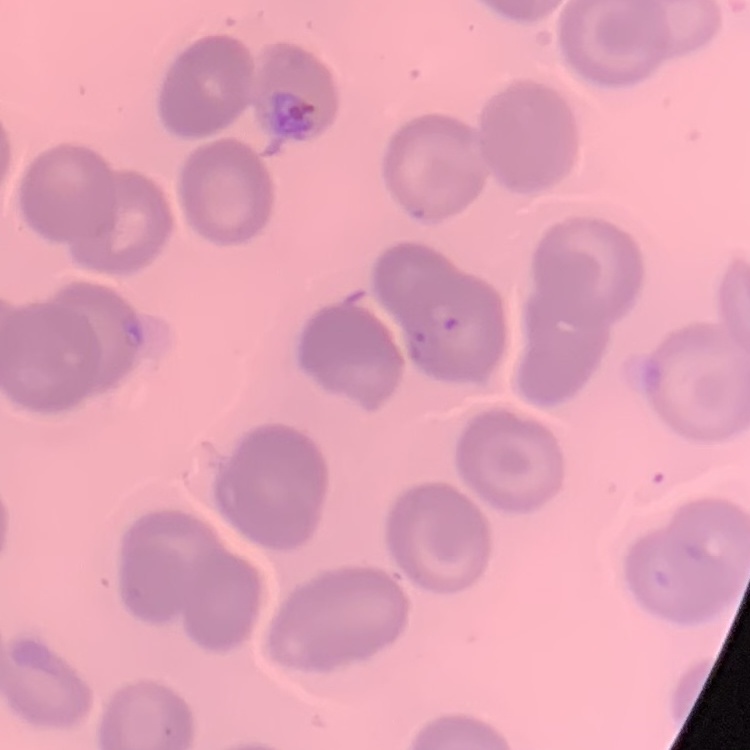
The red blood cells exhibit no rouleaux formation. Thin peripheral smear. Field's or Giemsa stain. Square crop of a larger photomicrograph.